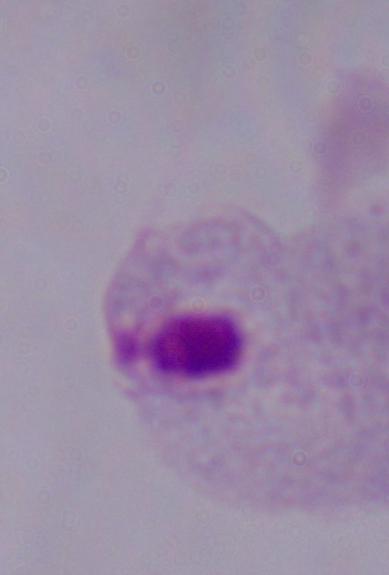
identification: trichomonad
modality: micrograph
magnification: 1000x